Name the parasite shown.
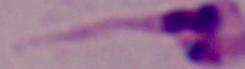
This is Leishmania.

magnification = 1000x
modality = photomicrograph